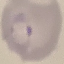

result = malaria parasites identified
capture = smartphone through the microscope eyepiece
image type = cell patch, automatically extracted from a larger field of view and resized to 64 × 64 pixels
preparation = thin blood smear
stain = Giemsa